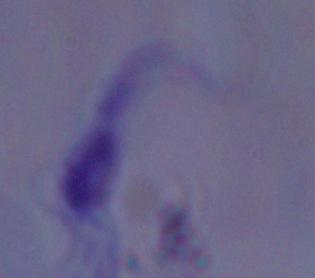

Summary:
  - Magnification: 1000x
  - Identification: trypanosome
  - Modality: photomicrograph